Identify the parasite.
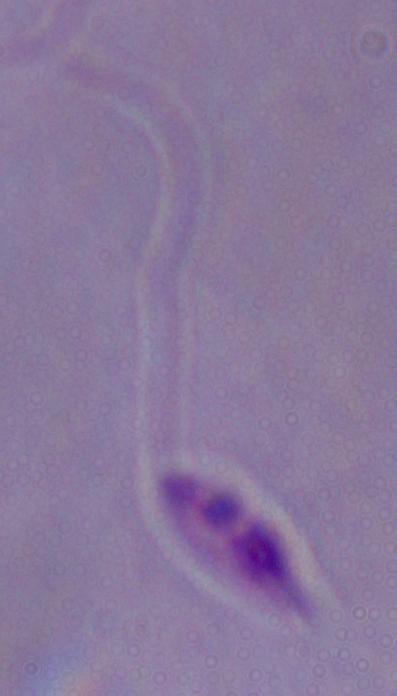
This is Leishmania.

Captured at 1000x magnification. Photomicrograph.